Describe the morphology of the red blood cells.
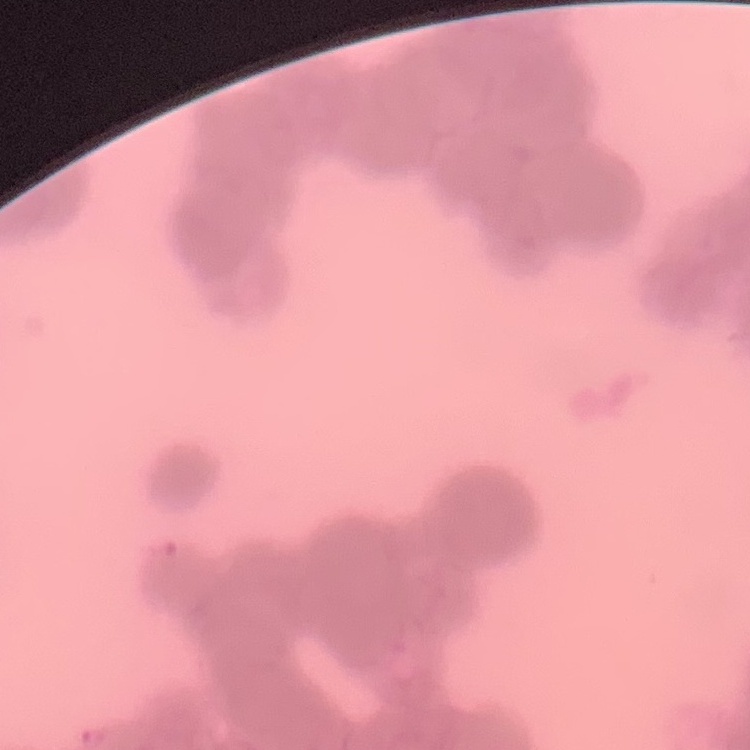
They show rouleaux formation.

Summary:
  - Stain: Field's or Giemsa
  - Preparation: thin peripheral smear
  - Image type: square crop of a larger photomicrograph